Name the cell type shown.
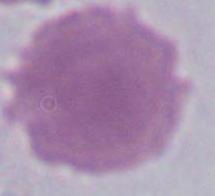
An erythrocyte.

{
  "magnification": "1000x",
  "modality": "photomicrograph"
}